Identify the preparation type.
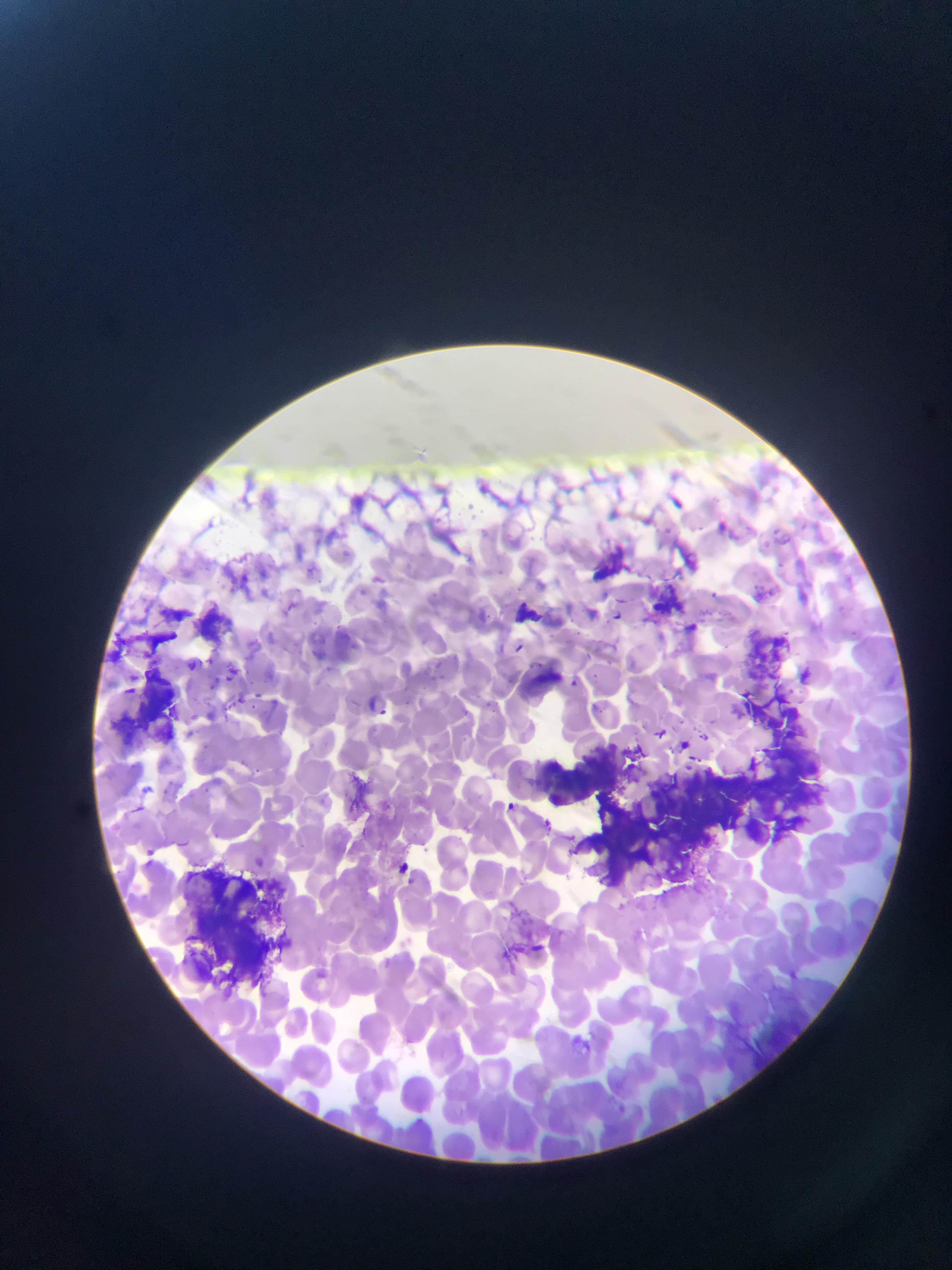

Thin blood film.

Approximate bounding boxes as {left, top, right, bottom} in pixels.
Summary:
  - Malaria parasite locations: {613, 611, 621, 621}, {515, 644, 524, 653}, {207, 656, 219, 669}, {225, 668, 238, 681}, {569, 680, 582, 687}, {379, 707, 392, 716}, {649, 723, 667, 741}, {508, 802, 518, 812}, {133, 806, 157, 816}, {541, 814, 557, 828}, {178, 842, 192, 848}
  - Artifact (stain precipitate or debris) locations: {590, 538, 635, 581}, {654, 578, 697, 631}, {153, 596, 191, 628}, {517, 597, 543, 624}, {190, 599, 235, 641}, {103, 616, 182, 673}, {741, 629, 818, 692}, {529, 661, 567, 693}, {107, 665, 180, 743}, {743, 691, 820, 768}, {537, 753, 644, 800}, {771, 757, 823, 840}, {697, 760, 783, 848}, {580, 781, 704, 886}, {177, 869, 289, 984}
  - Country: Ghana
  - Capture: mobile-phone photograph through a microscope
  - Image size: 952×1270 pixels
  - Field of view: single